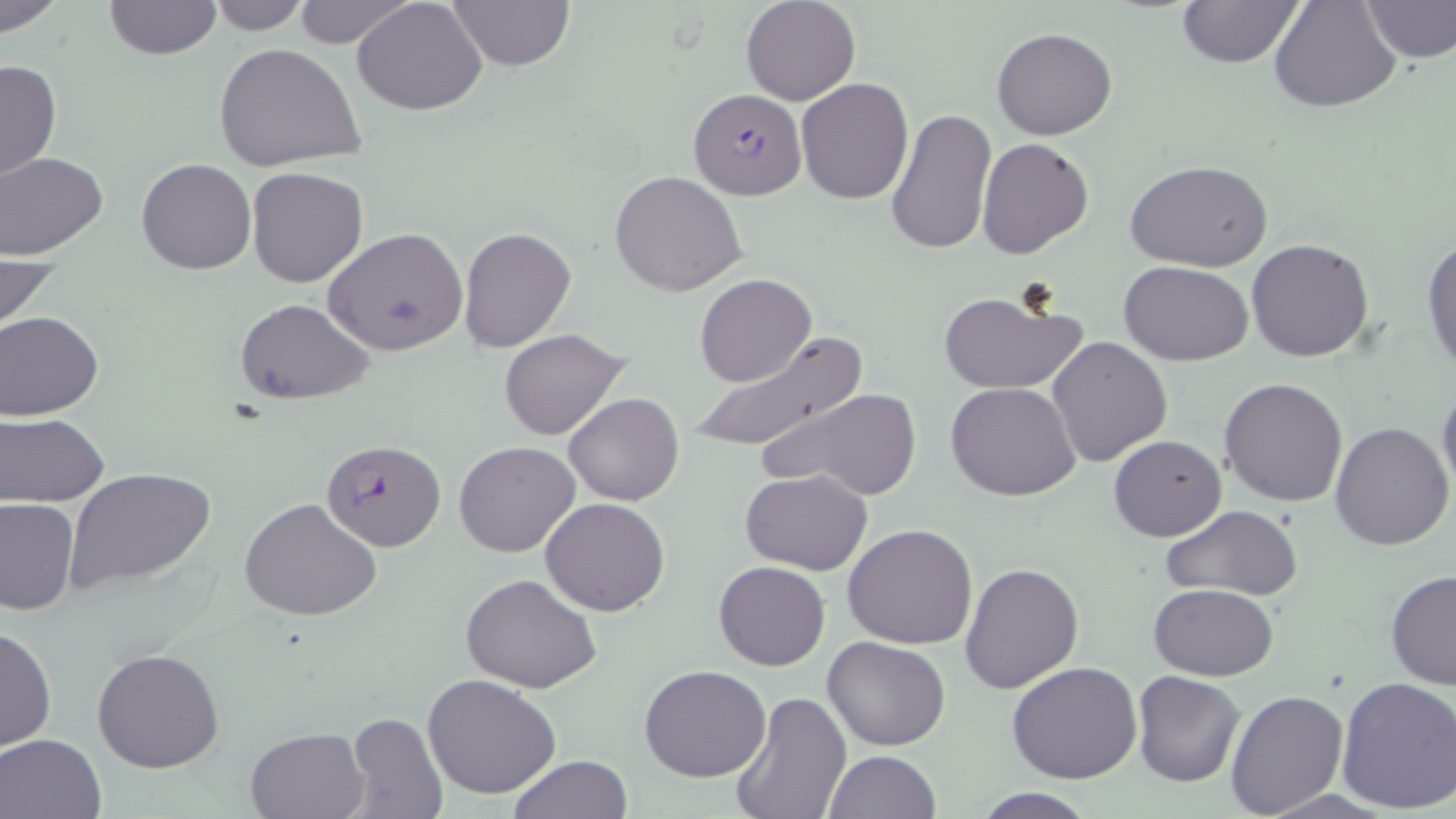

plasmodium_falciparum_infected_red_blood_cell_locations: 'approximate bounding boxes as (x1,y1)-(x2,y2) corner pairs in pixels: (689,88)-(807,200), (322,439)-(446,551)'
slide_level_diagnosis: Plasmodium falciparum
preparation: thin blood smear
stain: May-Grünwald-Giemsa
magnification: 1000x
modality: light microscopy
image_size: 1456×819 pixels
field_of_view: one of a larger specimen
uninfected_red_blood_cell_locations: 'approximate bounding boxes as (x1,y1)-(x2,y2) corner pairs in pixels: (0,0)-(67,36), (104,0)-(221,59), (290,0)-(416,48), (352,0)-(489,115), (446,0)-(575,70), (740,0)-(861,106), (1268,0)-(1400,113), (205,1)-(313,34), (1177,1)-(1304,68), (1363,1)-(1456,63), (991,28)-(1118,140), (215,44)-(369,174), (0,57)-(62,184), (795,78)-(915,205), (885,108)-(998,255), (976,137)-(1096,260), (0,150)-(109,261), (137,158)-(255,275), (1128,160)-(1273,273), (247,167)-(367,287), (609,170)-(749,297), (458,226)-(576,352), (324,227)-(469,358), (1421,237)-(1456,373), (1247,238)-(1376,362), (0,250)-(57,339), (1121,260)-(1254,365), (694,273)-(817,387), (936,288)-(1090,397), (233,298)-(375,404), (1,312)-(103,419), (501,328)-(631,441), (682,330)-(867,460), (1046,335)-(1173,468), (1219,377)-(1349,506), (1437,379)-(1456,500), (946,381)-(1080,501), (764,387)-(923,500), (565,393)-(684,507), (0,412)-(110,506), (1331,423)-(1454,551), (1109,434)-(1227,541), (454,440)-(581,557), (65,467)-(217,597), (741,468)-(874,575), (0,497)-(79,614), (241,497)-(383,622), (540,497)-(670,617), (1157,504)-(1305,600), (843,524)-(978,649), (714,561)-(831,670), (959,563)-(1084,694), (1386,568)-(1456,691), (462,574)-(604,695), (1149,583)-(1278,680), (1,624)-(56,754), (825,637)-(949,751), (93,646)-(224,774), (1008,660)-(1143,785), (641,665)-(771,782), (1131,671)-(1247,787), (423,674)-(560,800), (1335,676)-(1456,812), (1224,687)-(1349,816), (728,692)-(852,819), (344,710)-(447,819), (245,727)-(369,818), (1,732)-(106,818), (825,749)-(941,818), (509,755)-(634,818), (964,789)-(1103,818)'